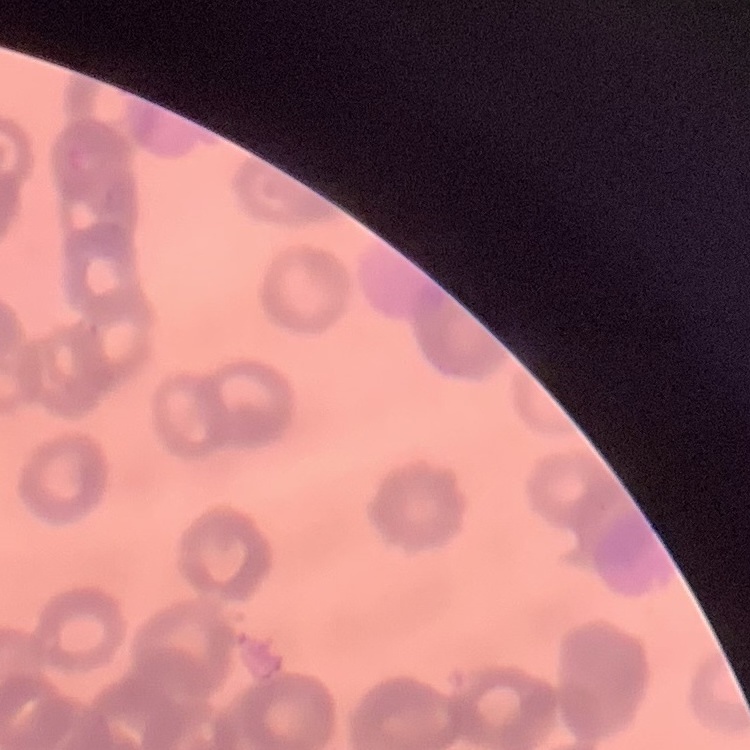

erythrocyte morphology = rouleaux formation
stain = Field's or Giemsa
image type = square crop of a larger photomicrograph
preparation = thin blood film